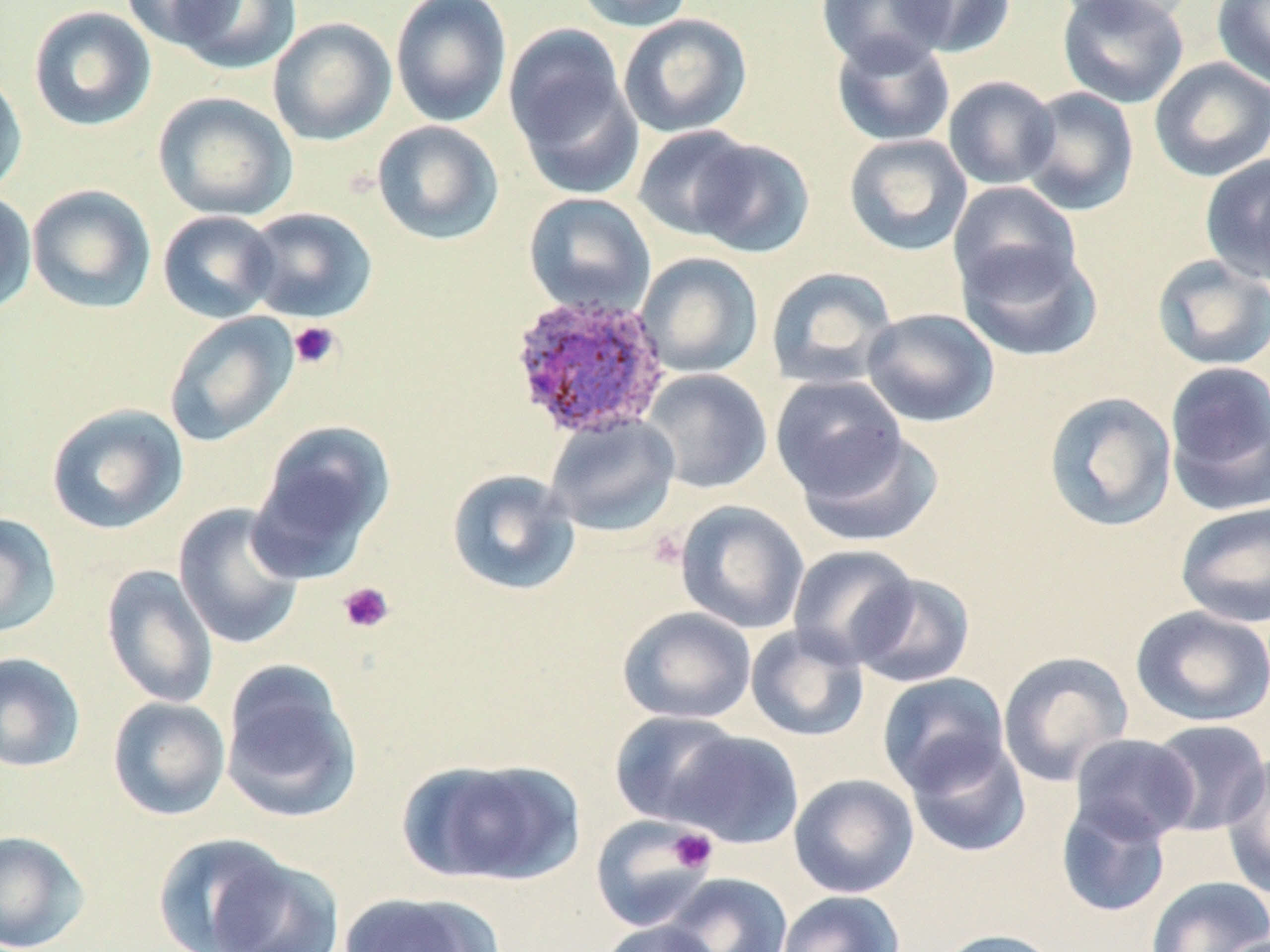

Summary:
  - Coordinate format: approximate bounding boxes as [x1, y1, x2, y2] in pixels
  - Plasmodium ovale-infected red blood cell locations: [508, 292, 674, 440]
  - Uninfected red blood cell locations: [120, 0, 240, 51], [171, 0, 301, 76], [390, 0, 512, 127], [572, 0, 696, 32], [893, 0, 1017, 57], [1056, 0, 1201, 27], [1057, 0, 1189, 109], [1211, 0, 1270, 89], [816, 1, 952, 71], [28, 5, 157, 131], [618, 13, 752, 138], [268, 17, 397, 146], [503, 23, 639, 188], [830, 33, 956, 148], [1149, 57, 1270, 182], [0, 69, 28, 200], [942, 75, 1059, 190], [1018, 86, 1140, 216], [153, 91, 298, 221], [371, 120, 505, 246], [632, 125, 760, 243], [844, 133, 973, 256], [691, 137, 816, 258], [1200, 154, 1270, 285], [947, 181, 1083, 298], [26, 184, 157, 314], [0, 190, 37, 317], [523, 192, 656, 318], [241, 207, 378, 323], [157, 210, 280, 323], [955, 239, 1103, 363], [635, 252, 763, 378], [1151, 254, 1270, 371], [764, 266, 899, 390], [861, 307, 1000, 428], [163, 311, 299, 447], [1163, 360, 1270, 514], [640, 368, 772, 494], [772, 375, 907, 501], [1042, 391, 1178, 533], [45, 403, 188, 535], [544, 414, 680, 537], [252, 419, 396, 570], [795, 428, 943, 548], [446, 468, 581, 596], [675, 500, 809, 634], [1174, 501, 1270, 628], [173, 502, 307, 650], [0, 512, 62, 639], [787, 544, 919, 668], [101, 564, 219, 708], [851, 573, 976, 688], [1130, 605, 1270, 728], [617, 606, 757, 725], [745, 624, 869, 742], [997, 650, 1135, 787], [0, 652, 86, 773], [219, 659, 363, 824], [877, 672, 1011, 795], [107, 696, 231, 821], [609, 710, 746, 827], [1148, 718, 1270, 836], [670, 730, 804, 849], [1068, 733, 1200, 844], [905, 736, 1032, 858], [1221, 752, 1270, 898], [399, 756, 585, 887], [788, 774, 919, 898], [1056, 798, 1173, 918], [589, 815, 717, 932], [0, 829, 91, 952], [150, 832, 298, 952], [207, 855, 346, 952], [662, 872, 793, 952], [1145, 875, 1270, 952], [776, 890, 904, 952], [337, 891, 503, 952], [597, 919, 725, 952], [934, 928, 1064, 952], [1212, 933, 1270, 952]
  - Platelet locations: [288, 321, 341, 370], [337, 582, 395, 634], [669, 828, 717, 873]
  - Slide-level diagnosis: Plasmodium ovale
  - Preparation: thin blood smear
  - Modality: light microscopy
  - Image size: 1270×952 pixels
  - Stain: May-Grünwald-Giemsa
  - Magnification: 1000x
  - Field of view: single